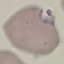

malaria status = parasitized
preparation = thin blood film
capture = smartphone camera at the microscope eyepiece
image type = cell patch, automatically extracted from a larger field of view and resized to 64 × 64 pixels
stain = Giemsa